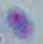 Toxoplasma gondii is shown. Micrograph. Captured at 1000x magnification.